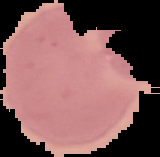

Summary:
  - Result: Plasmodium parasites identified
  - Image type: segmented cell region on a black background
  - Image size: 160×157 pixels
  - Preparation: thin blood film